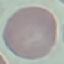

Result: negative for malaria parasites. Automatically extracted cell patch, resized to 64 × 64 pixels. Giemsa stain. Thin smear of blood. Photographed with a smartphone camera at the microscope eyepiece.